Locate every blood parasite and identify its species.
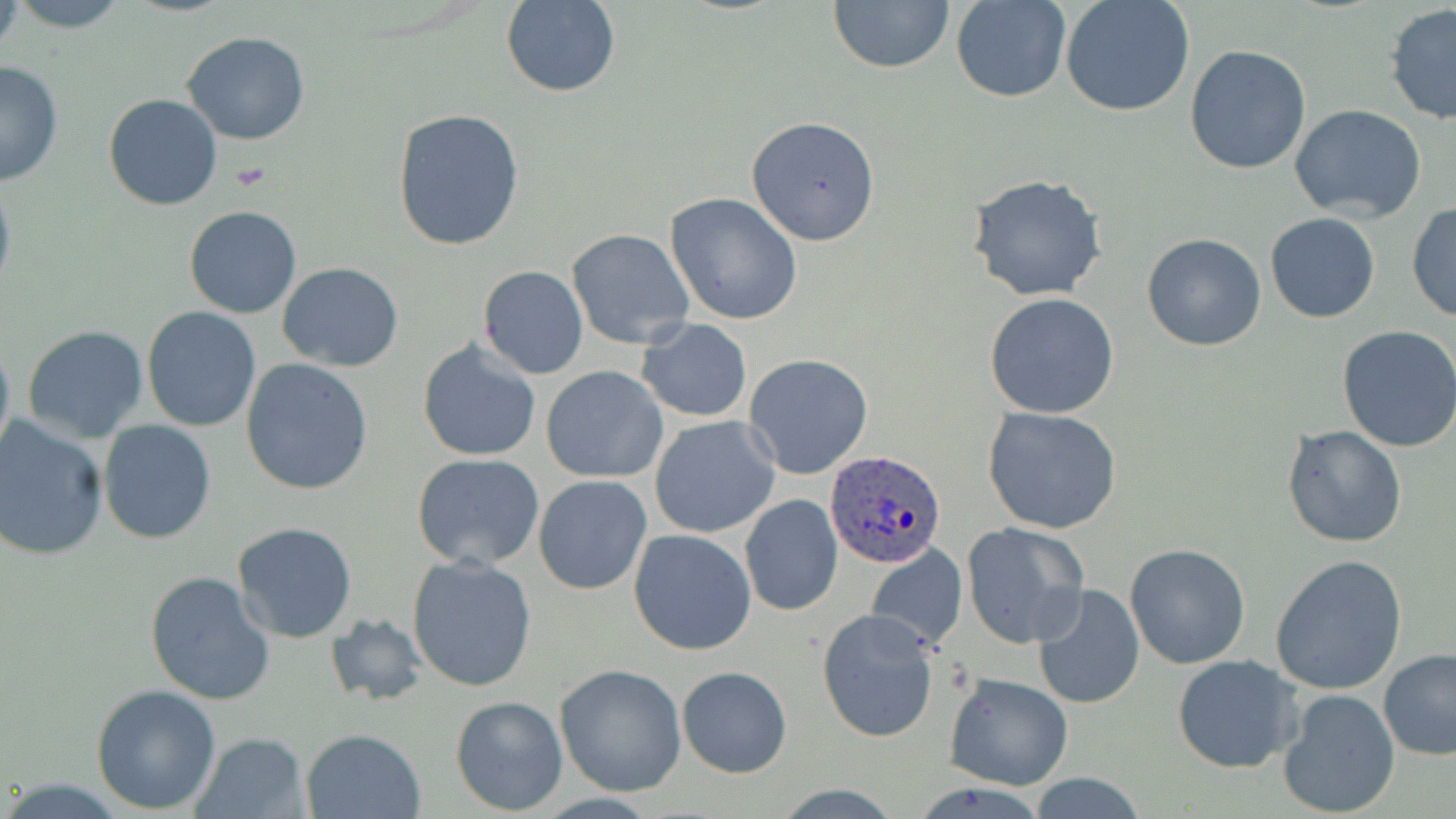

Approximate bounding boxes as named x1/y1/x2/y2 corners in pixels.
Plasmodium ovale-infected red blood cells: (x1=826, y1=450, x2=946, y2=570).
No Plasmodium falciparum, Plasmodium malariae, Plasmodium vivax, Babesia divergens, or Trypanosoma brucei observed.

{
  "slide_level_diagnosis": "Plasmodium ovale",
  "platelet_locations": "approximate bounding boxes as named x1/y1/x2/y2 corners in pixels: (x1=231, y1=162, x2=270, y2=190)",
  "uninfected_red_blood_cell_locations": "approximate bounding boxes as named x1/y1/x2/y2 corners in pixels: (x1=8, y1=0, x2=133, y2=31), (x1=829, y1=0, x2=955, y2=72), (x1=952, y1=0, x2=1071, y2=102), (x1=1060, y1=0, x2=1195, y2=117), (x1=502, y1=1, x2=619, y2=97), (x1=1384, y1=5, x2=1456, y2=127), (x1=182, y1=31, x2=311, y2=146), (x1=1185, y1=45, x2=1312, y2=174), (x1=0, y1=61, x2=64, y2=188), (x1=103, y1=94, x2=222, y2=211), (x1=1289, y1=104, x2=1427, y2=223), (x1=392, y1=107, x2=527, y2=254), (x1=745, y1=116, x2=881, y2=245), (x1=0, y1=168, x2=16, y2=308), (x1=967, y1=172, x2=1110, y2=304), (x1=666, y1=192, x2=804, y2=324), (x1=1407, y1=200, x2=1456, y2=324), (x1=184, y1=205, x2=301, y2=318), (x1=1265, y1=212, x2=1380, y2=323), (x1=568, y1=228, x2=695, y2=349), (x1=1141, y1=234, x2=1267, y2=351), (x1=278, y1=263, x2=403, y2=370), (x1=477, y1=266, x2=588, y2=379), (x1=442, y1=275, x2=571, y2=432), (x1=983, y1=293, x2=1120, y2=419), (x1=141, y1=306, x2=264, y2=432), (x1=638, y1=319, x2=752, y2=422), (x1=21, y1=325, x2=149, y2=444), (x1=1337, y1=326, x2=1456, y2=451), (x1=0, y1=330, x2=15, y2=464), (x1=417, y1=339, x2=543, y2=463), (x1=743, y1=353, x2=874, y2=479), (x1=240, y1=359, x2=373, y2=495), (x1=541, y1=366, x2=668, y2=484), (x1=982, y1=405, x2=1124, y2=535), (x1=0, y1=416, x2=108, y2=561), (x1=649, y1=416, x2=781, y2=539), (x1=97, y1=420, x2=217, y2=544), (x1=1281, y1=425, x2=1408, y2=549), (x1=410, y1=452, x2=545, y2=570), (x1=533, y1=476, x2=652, y2=594), (x1=739, y1=494, x2=844, y2=618), (x1=231, y1=522, x2=359, y2=644), (x1=961, y1=522, x2=1089, y2=648), (x1=629, y1=527, x2=755, y2=656), (x1=866, y1=543, x2=967, y2=653), (x1=1125, y1=543, x2=1252, y2=669), (x1=406, y1=554, x2=538, y2=692), (x1=1270, y1=555, x2=1407, y2=695), (x1=143, y1=572, x2=276, y2=705), (x1=1030, y1=585, x2=1144, y2=710), (x1=816, y1=608, x2=940, y2=744), (x1=324, y1=614, x2=429, y2=706), (x1=1378, y1=650, x2=1456, y2=760), (x1=1171, y1=654, x2=1302, y2=773), (x1=555, y1=664, x2=688, y2=797), (x1=678, y1=666, x2=791, y2=777), (x1=943, y1=671, x2=1073, y2=790), (x1=90, y1=684, x2=221, y2=813), (x1=1276, y1=688, x2=1402, y2=815), (x1=450, y1=695, x2=569, y2=816), (x1=299, y1=727, x2=426, y2=819), (x1=189, y1=733, x2=309, y2=819), (x1=1027, y1=775, x2=1146, y2=818), (x1=770, y1=782, x2=906, y2=817)",
  "stain": "May-Grünwald-Giemsa",
  "preparation": "thin blood film",
  "field_of_view": "one of a larger specimen",
  "magnification": "1000x",
  "image_size": "1456×819 pixels",
  "modality": "optical microscopy"
}